Classify this cell by malaria status.
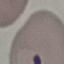

It is parasitized.

Photographed with a smartphone camera at the microscope eyepiece. Thin smear of blood. Giemsa stain. Automatically extracted cell patch, resized to 64 × 64 pixels.